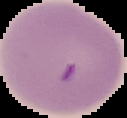
preparation = thin blood smear
image size = 127×118 pixels
result = no Plasmodium parasites seen
image type = cell region segmented out of the field of view; surrounding area masked to black